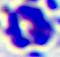
Summary:
  - Identification: white blood cell
  - Modality: micrograph
  - Magnification: 400x